Report the malaria status of this cell.
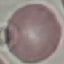
Uninfected.

preparation = thin blood film
stain = Giemsa
image type = automatically extracted cell patch, resized to 64 × 64 pixels
capture = smartphone through the microscope eyepiece